Report the malaria status of this cell.
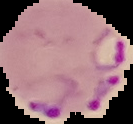
It is parasitized.

preparation = thin blood smear
image type = segmented cell region with the area outside set to black
image size = 133×124 pixels